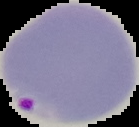
Image is 139×127 pixels. The area outside the segmented cell region is set to black. From a thin blood film. Malaria status: parasitized.